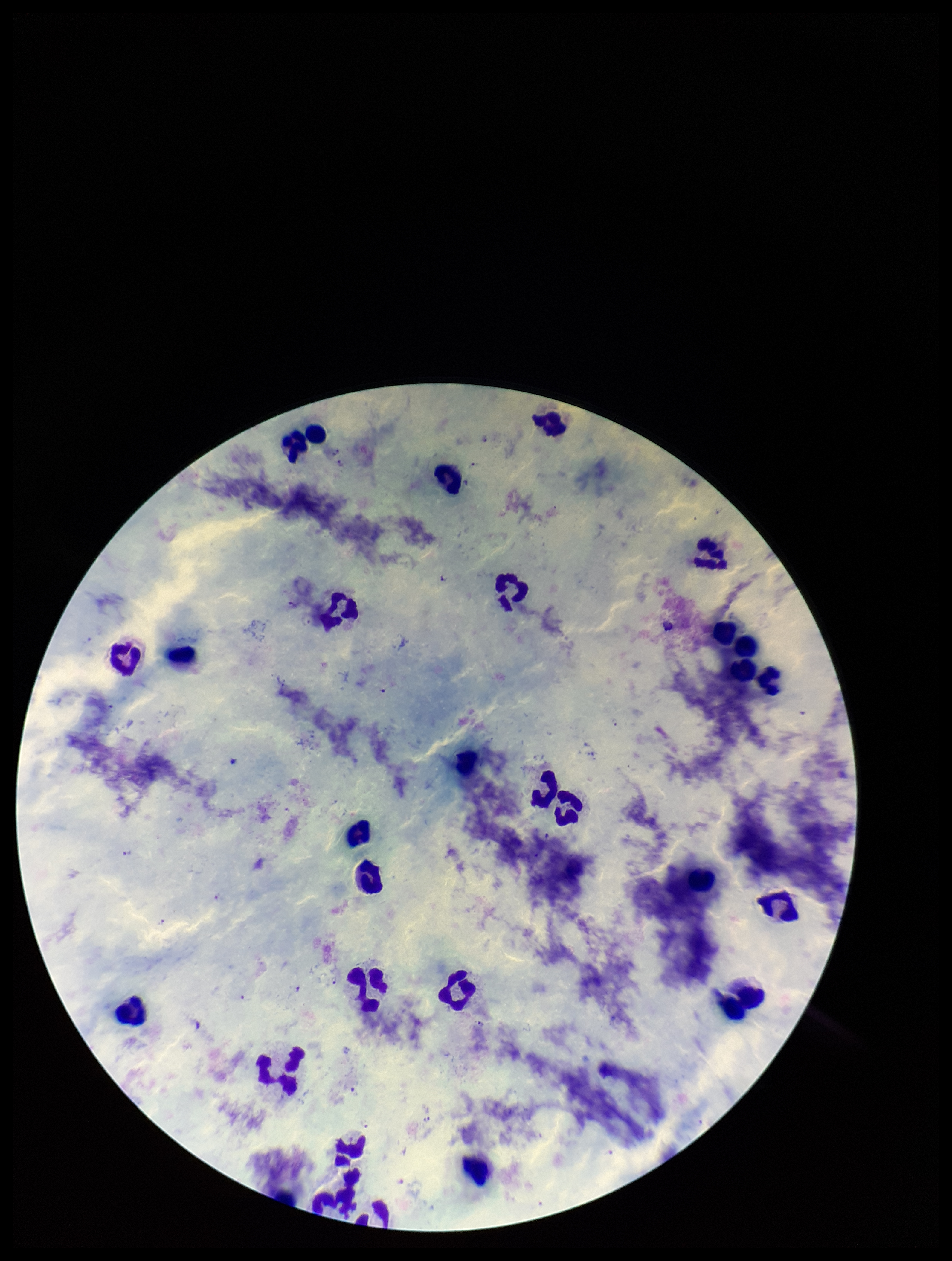

Summary:
  - Parasite count: 11
  - Field of view: single
  - Stain: Giemsa
  - Patient malaria status: positive
  - Preparation: thick blood smear
  - Image size: 952×1261 pixels
  - Plasmodium parasites: detected
  - Leukocyte count: 28
  - Capture: smartphone photograph through the microscope eyepiece
  - Species reported for this patient: Plasmodium falciparum